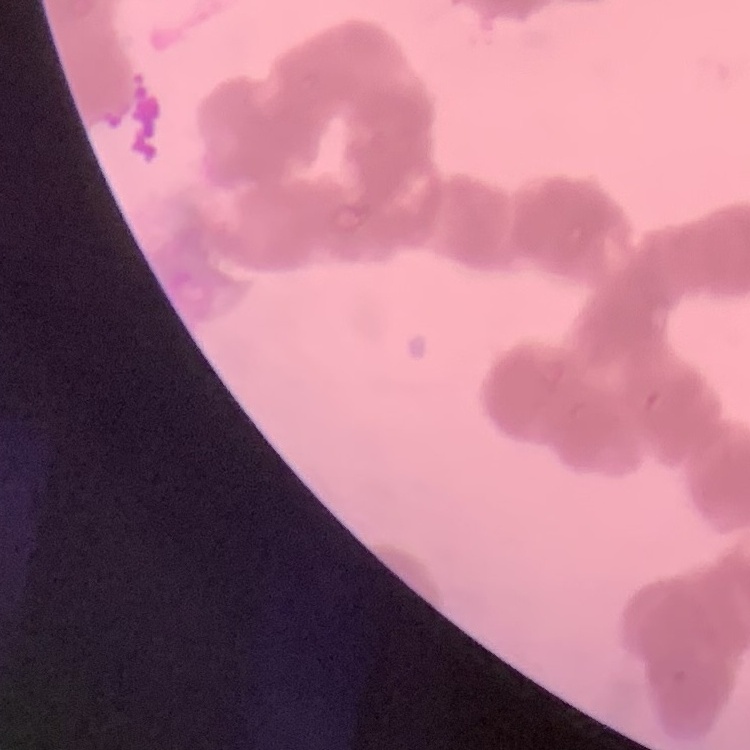
Summary:
  - Erythrocyte morphology: rouleaux formation
  - Image type: one tile cut from a larger photomicrograph
  - Preparation: thin peripheral smear
  - Stain: Field's or Giemsa